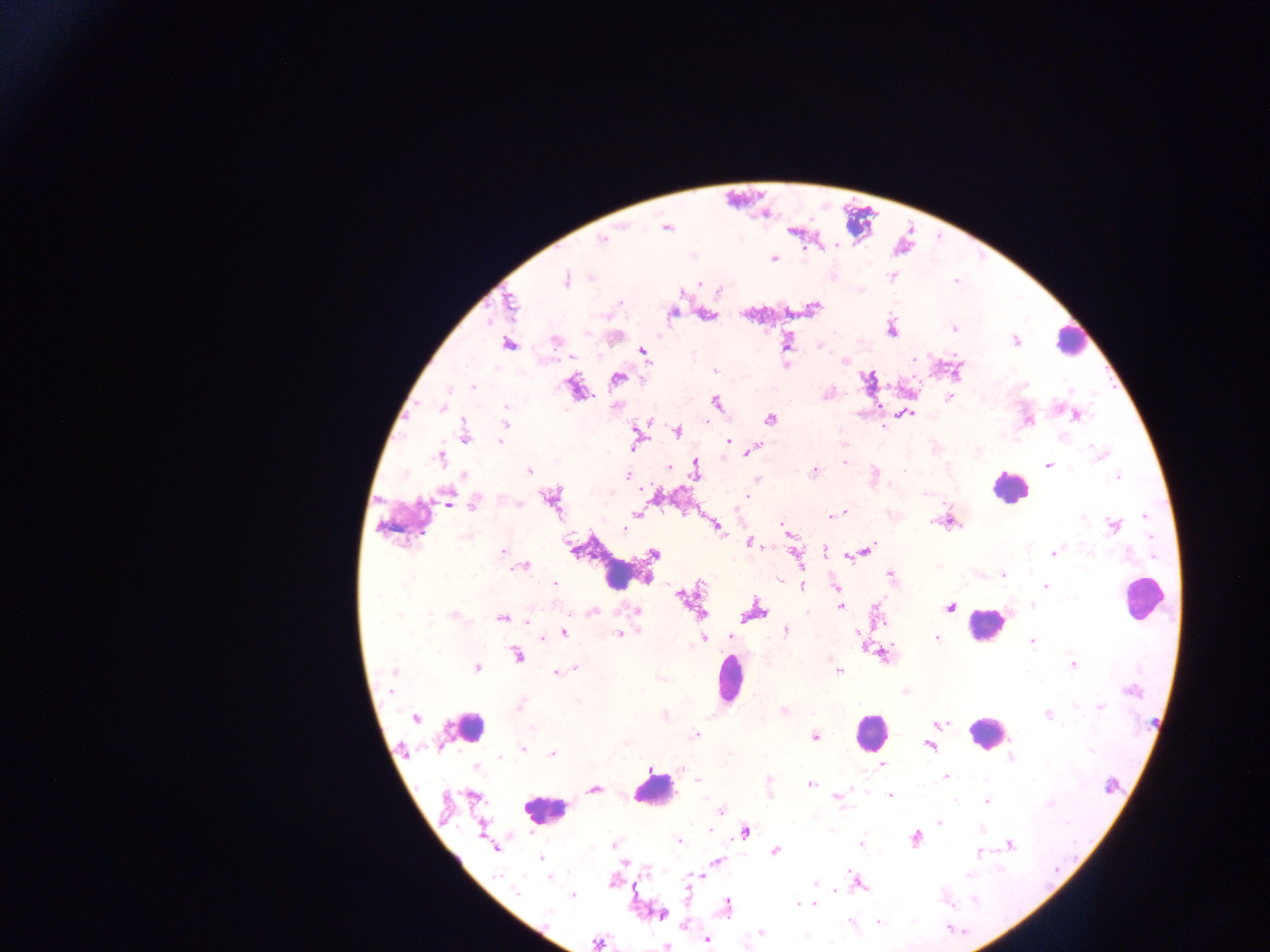 Approximate centers as x y in pixels. Malaria parasite locations: 666 226; 602 241; 774 258; 565 279; 699 283; 509 304; 811 308; 671 313; 707 315; 953 327; 891 329; 1015 341; 787 342; 507 343; 642 351; 843 359; 714 370; 957 370; 617 377; 867 380; 474 386; 1024 386; 573 387; 828 393; 948 398; 716 402; 442 407; 906 413; 1075 414; 769 418; 647 420; 1028 420; 504 423; 885 425; 677 431; 464 436; 635 439; 499 440; 726 442; 754 448; 1102 455; 440 457; 845 463; 1048 464; 669 467; 695 469; 528 470; 813 471; 874 473; 628 475; 1118 477; 756 479; 746 495; 550 497; 449 499; 518 502; 475 503; 636 513; 841 513; 836 515; 831 516; 948 520; 1114 525; 716 526; 785 526; 623 529; 787 532; 750 541; 864 550; 502 551; 825 551; 856 551; 1053 553; 654 554; 849 555; 797 559; 522 566; 1002 574; 890 576; 554 584; 801 586; 1045 586; 836 588; 681 595; 839 606; 950 606; 635 610; 700 610; 591 611; 753 612; 453 615; 502 617; 527 621; 785 629; 562 633; 620 633; 540 636; 704 638; 730 638; 936 638; 862 640; 1031 641; 883 653; 516 654; 1073 664; 476 667; 574 668; 392 671; 838 671; 556 672; 906 692; 520 705; 1100 707; 783 710; 1048 715; 416 718; 939 723; 695 735; 814 736; 929 745; 522 750; 553 754; 1011 757; 881 765; 945 776; 697 781; 810 784; 1109 785; 594 789; 837 796; 890 796; 987 801; 720 809; 939 820; 481 828; 709 829; 980 829; 744 831; 916 837; 678 841; 861 843; 1009 843; 614 845; 495 847; 774 850; 978 853; 542 858; 718 862; 550 876; 700 876; 852 877; 613 881; 856 881; 815 883; 836 890; 517 891; 688 892; 573 894; 798 901; 806 903; 814 903; 727 906; 660 914; 850 922; 685 925; 760 932; 707 939; 597 943; 666 945. Leukocyte locations: 1070 340; 1010 486; 403 523; 625 570; 1143 598; 986 626; 728 678; 466 727; 870 732; 987 733; 653 789; 544 809. Image is 1270×952 pixels. Single field of view. Thick blood smear. Mobile-phone photograph taken through the microscope. Collected in Ghana.